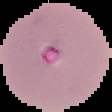 From a thin blood smear. The area outside the segmented cell region is set to black. Result: Plasmodium parasites detected. Image is 112×112 pixels.